Assess this cell for malaria.
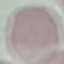

Uninfected.

image_type: cell patch, automatically extracted from a larger field of view and resized to 64 × 64 pixels
stain: Giemsa
preparation: thin smear
capture: smartphone camera at the microscope eyepiece